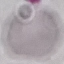

result = no malaria parasites seen
capture = smartphone camera at the microscope eyepiece
image type = cell patch, automatically extracted from a larger field of view and resized to 64 × 64 pixels
preparation = thin smear
stain = Giemsa